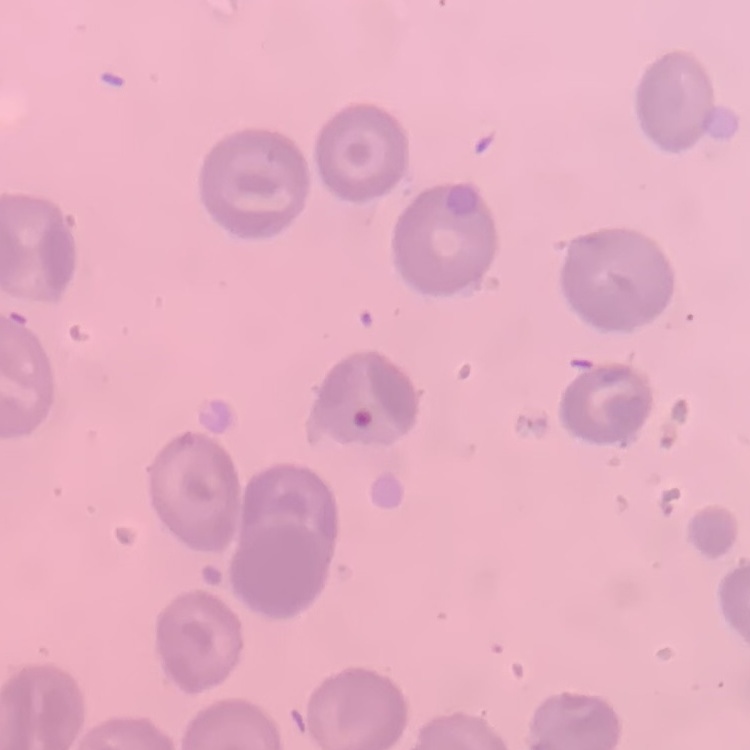
The red blood cells show no rouleaux formation. Thin blood film. Stained with either Field's or Giemsa. One tile cut from a larger photomicrograph.